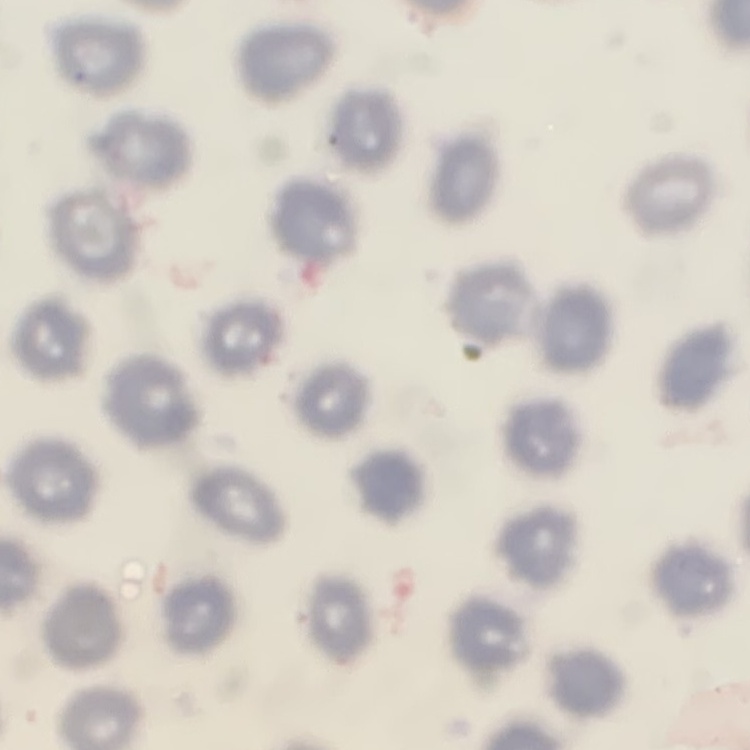

The red blood cells show no rouleaux formation. Square crop of a larger photomicrograph. Stained with either Field's or Giemsa. Thin peripheral smear.